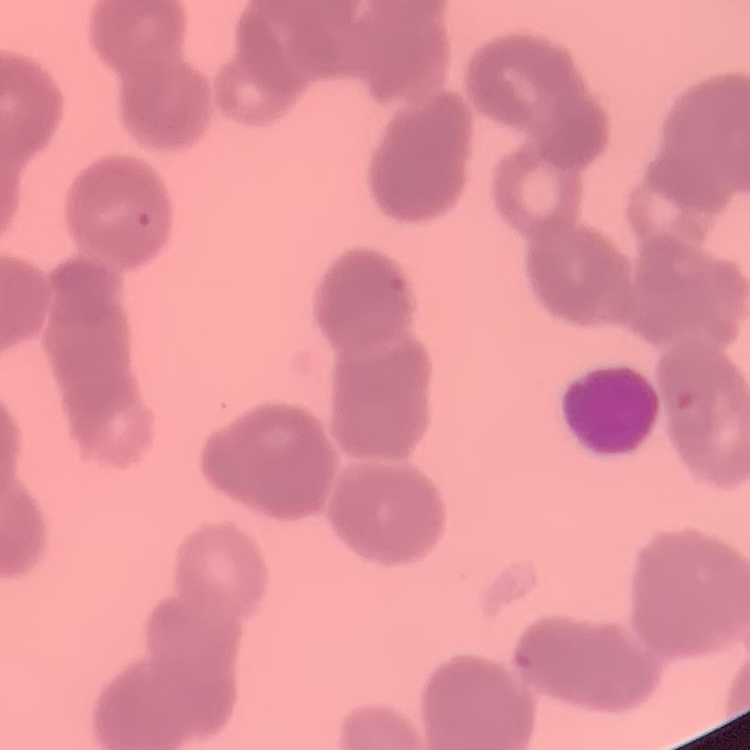

Summary:
  - Erythrocyte morphology: rouleaux formation
  - Preparation: thin blood film
  - Stain: Field's or Giemsa
  - Image type: square crop of a larger photomicrograph